Point out each leukocyte.
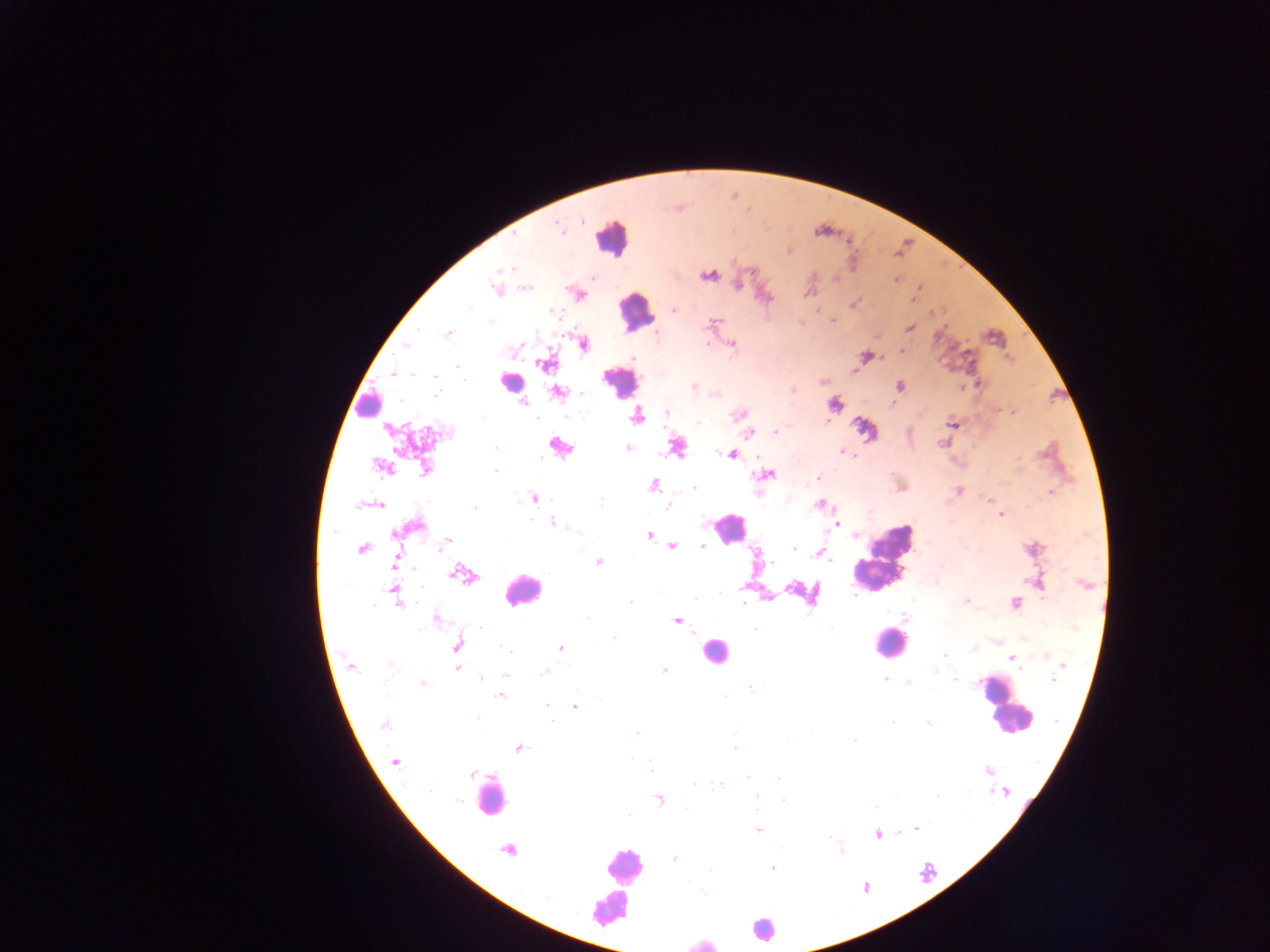
Approximate centers as [x, y] in pixels.
Leukocytes: [611, 238], [635, 312], [620, 381], [509, 382], [368, 402], [728, 528], [883, 559], [522, 590], [891, 643], [714, 652], [1007, 705], [489, 797], [624, 865], [617, 885], [604, 911], [763, 928], [701, 942].

Plasmodium parasite locations: [559, 228], [788, 251], [510, 268], [708, 274], [895, 279], [496, 289], [917, 291], [576, 293], [914, 296], [853, 303], [673, 311], [832, 320], [713, 323], [909, 327], [449, 333], [583, 344], [731, 344], [407, 346], [900, 351], [866, 356], [546, 362], [852, 370], [393, 374], [823, 381], [979, 383], [899, 385], [693, 386], [792, 389], [556, 392], [520, 401], [835, 404], [1012, 411], [666, 412], [739, 414], [637, 415], [952, 423], [866, 428], [390, 429], [749, 432], [775, 432], [943, 442], [559, 445], [496, 447], [628, 448], [676, 448], [841, 451], [731, 453], [381, 466], [426, 468], [495, 471], [765, 474], [818, 478], [653, 484], [694, 488], [957, 491], [1050, 492], [533, 497], [989, 500], [373, 504], [667, 504], [820, 504], [1000, 515], [552, 523], [834, 523], [414, 526], [648, 534], [445, 543], [671, 546], [702, 546], [1031, 548], [361, 549], [794, 549], [819, 553], [598, 561], [395, 563], [462, 574], [394, 591], [767, 597], [966, 600], [630, 601], [1014, 603], [435, 618], [677, 620], [614, 638], [457, 645], [972, 647], [560, 648], [944, 654], [1045, 655], [1011, 657], [1061, 663], [350, 667], [456, 669], [663, 670], [546, 671], [505, 675], [481, 678], [884, 678], [954, 679], [908, 682], [423, 684], [750, 687], [501, 694], [547, 704], [575, 706], [551, 721], [383, 724], [928, 724], [637, 732], [519, 748], [735, 748], [394, 762], [987, 770], [470, 773], [693, 783], [720, 785], [1004, 791], [659, 798], [915, 828], [758, 829], [877, 834], [508, 849], [673, 858], [772, 868]. Collected in Ghana. One field of view. Thick blood smear. Image is 1270×952 pixels. Mobile-phone photograph taken through the microscope.